Describe the morphology of the erythrocytes.
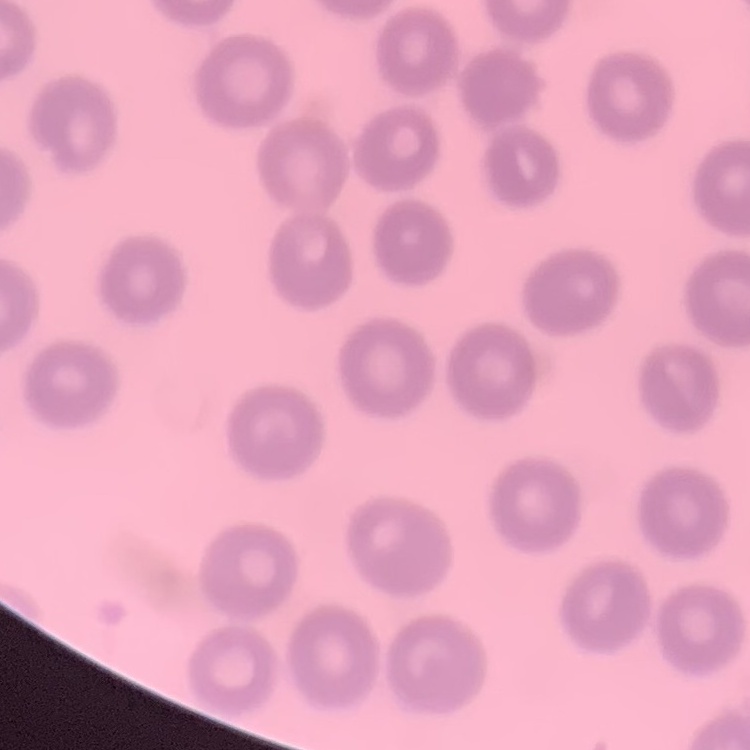

No rouleaux formation.

Summary:
  - Stain: Field's or Giemsa
  - Preparation: thin peripheral smear
  - Image type: square crop of a larger photomicrograph